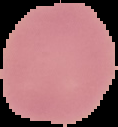

From a thin blood smear. Image is 118×127 pixels. Segmented cell region on a black background. Malaria status: uninfected.